State which parasite is depicted.
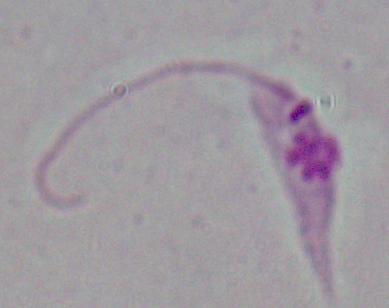
This is Leishmania.

magnification: 1000x
modality: photomicrograph